Comment on the morphology of the red blood cells.
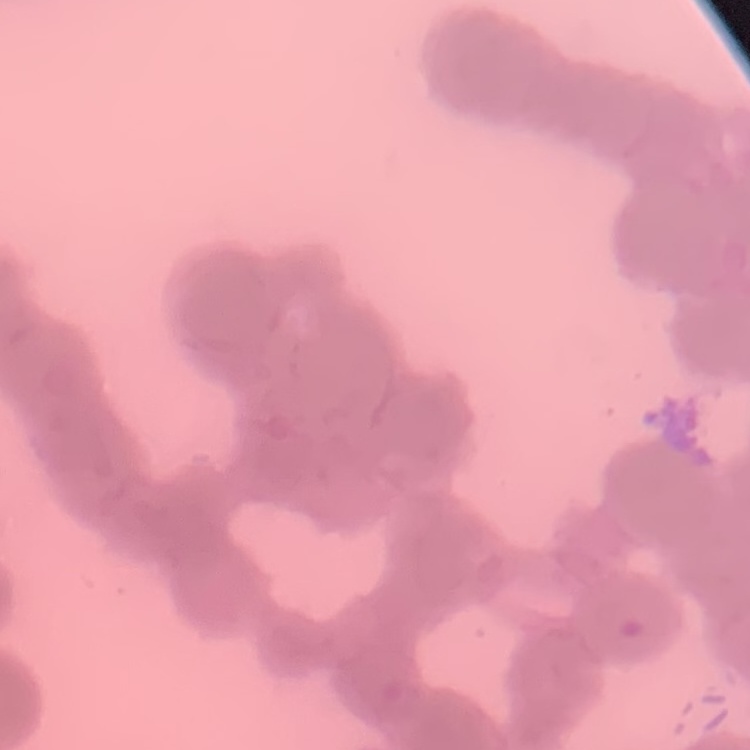

They show rouleaux formation.

Thin blood film. One tile cut from a larger photomicrograph. Stained with either Field's or Giemsa.